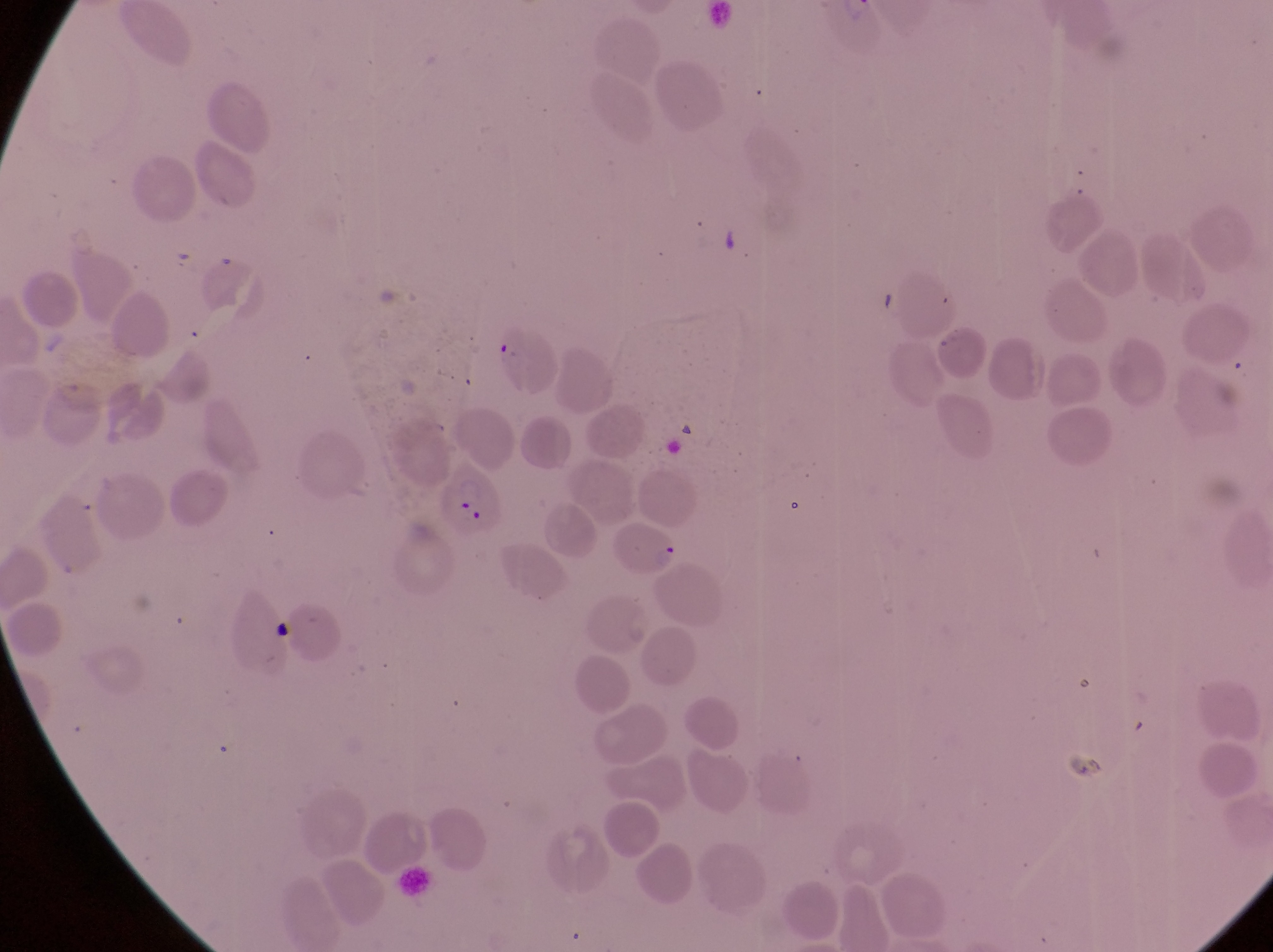

Approximate bounding boxes as [left, top, right, bottom] in pixels. Parasitised red blood cell locations: [439, 462, 504, 542]. At a magnification of 1000x. Photographed through the eyepiece of an Olympus CX-23 microscope with a smartphone camera. Image is 1273×952 pixels. Single field of view. Collected in Uganda. Thin blood smear.